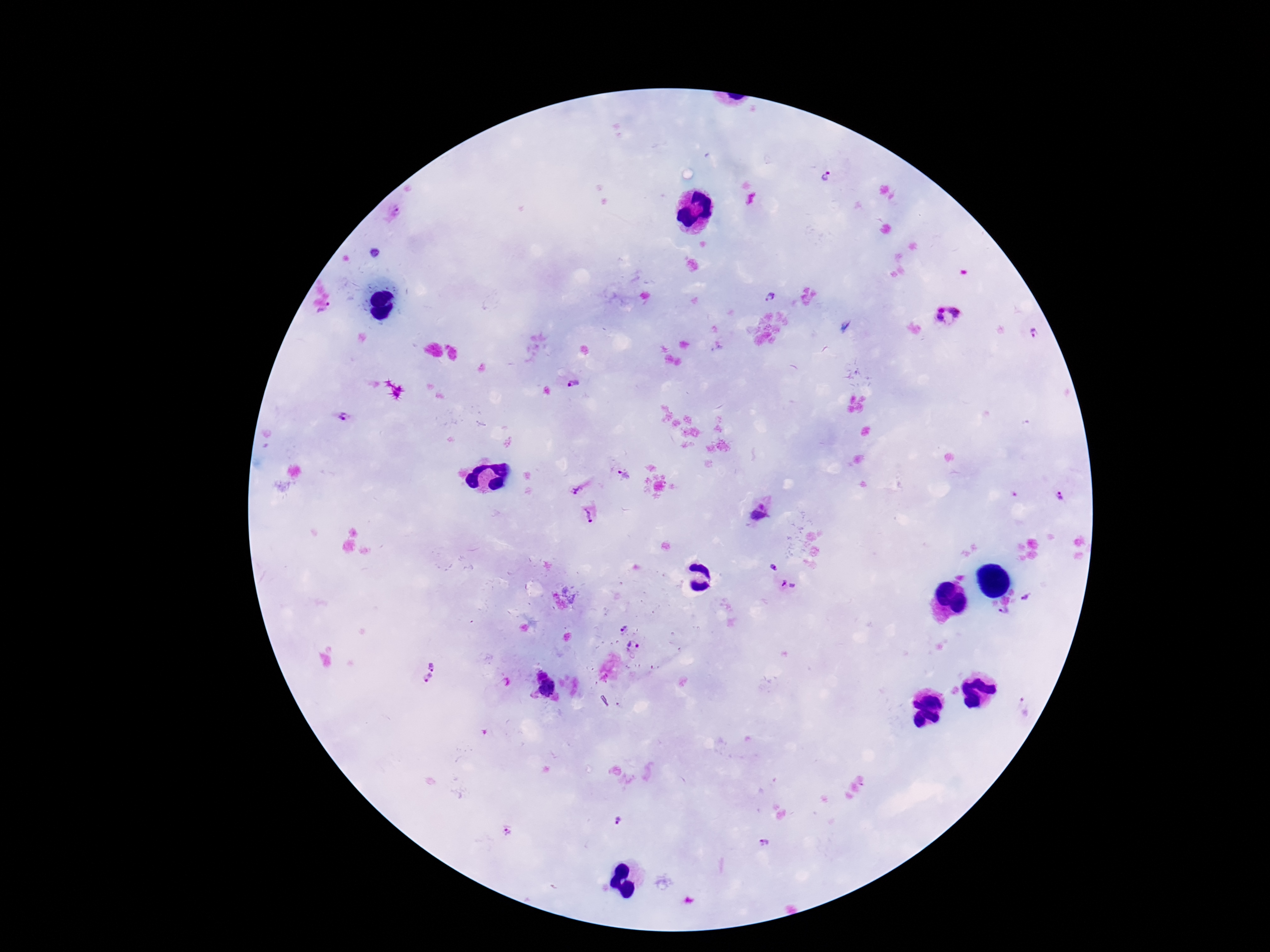

Approximate object centers, in pixels from the top-left corner. Plasmodium parasite locations: (x=827, y=178), (x=398, y=213), (x=772, y=297), (x=948, y=316), (x=1035, y=332), (x=574, y=382), (x=343, y=417), (x=625, y=475), (x=574, y=489), (x=1058, y=496), (x=759, y=513), (x=588, y=515), (x=774, y=568), (x=789, y=586), (x=1027, y=598), (x=1004, y=612), (x=624, y=628), (x=634, y=646), (x=432, y=666), (x=427, y=678), (x=1024, y=707), (x=618, y=820), (x=763, y=842). Smartphone photograph taken through the microscope eyepiece. Image is 1270×952 pixels. Giemsa-stained preparation. Patient malaria status: positive. Single field of view. Thick blood film. 100x magnification.